Give the position of every Plasmodium parasite visible.
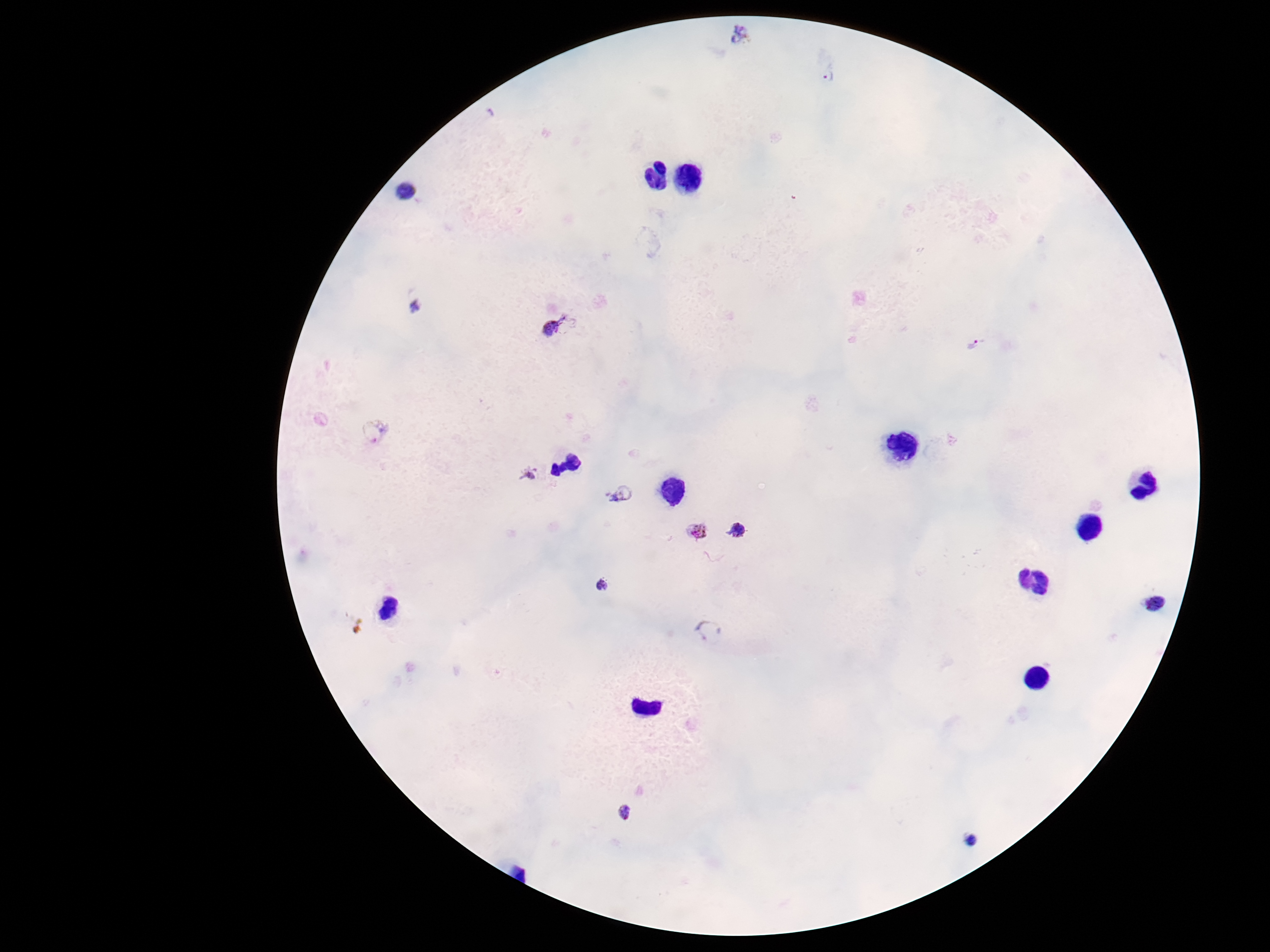

Approximate object centers, in pixels from the top-left corner.
Plasmodium parasites: (x=742, y=36), (x=828, y=76), (x=415, y=306), (x=561, y=326), (x=976, y=344), (x=375, y=431), (x=529, y=475), (x=621, y=495), (x=741, y=530), (x=698, y=532), (x=602, y=586), (x=1153, y=604), (x=708, y=630), (x=626, y=813), (x=971, y=840).

Image is 1270×952 pixels. Smartphone photograph taken through the microscope eyepiece. 100x magnification. Single field of view. Patient malaria status: positive. Thick blood film. Giemsa-stained preparation.